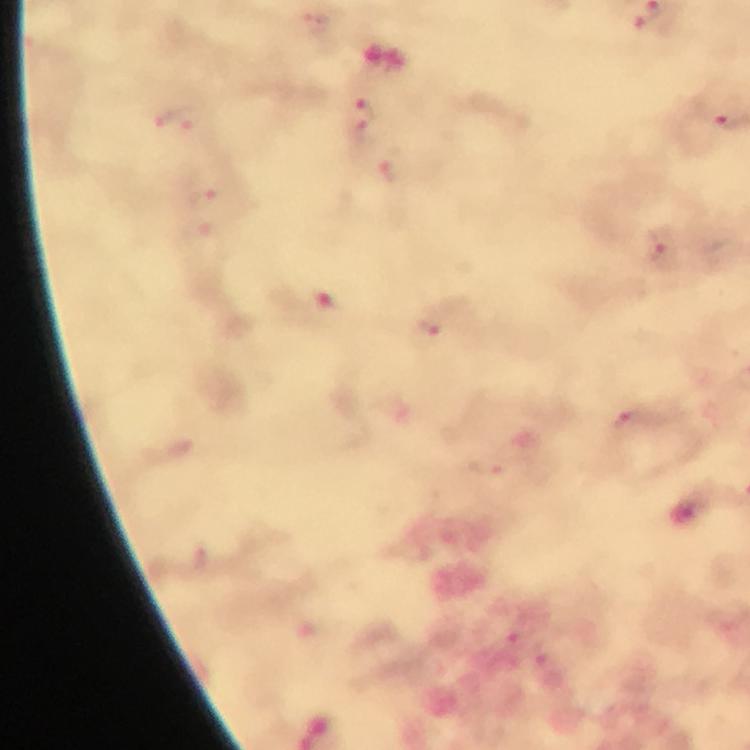
{
  "plasmodium_parasite_locations": "approximate centers as [x, y] in pixels: [360, 118], [174, 119], [208, 214], [662, 251], [430, 328], [630, 422]",
  "immersion_oil": "used",
  "capture": "smartphone mounted on the microscope",
  "context": "from a diagnostic examination for malaria",
  "cropped_from": "one field of view",
  "image_size": "750×750 pixels",
  "preparation": "thick blood film",
  "stain": "Giemsa",
  "magnification": "100x"
}